Give the position of every Plasmodium parasite.
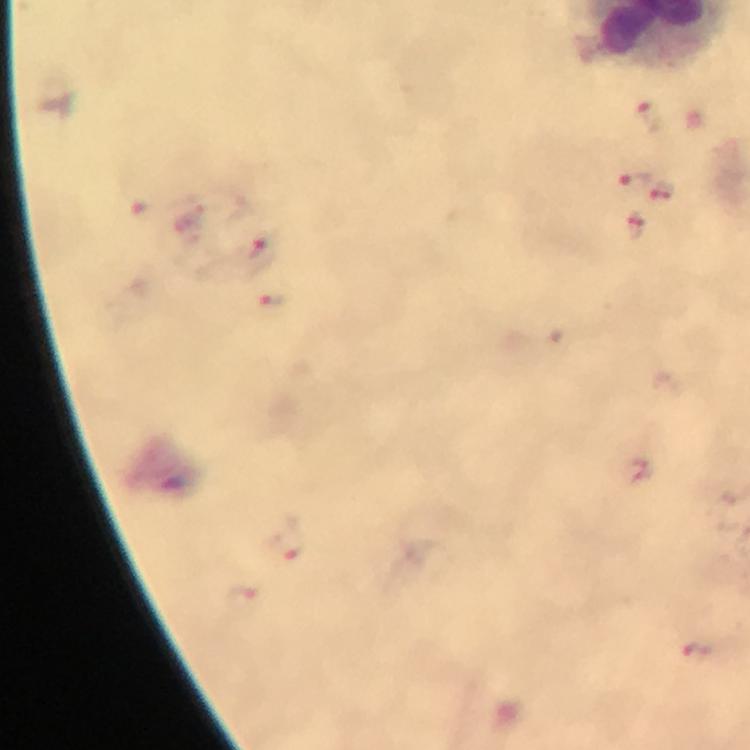

Approximate centers as {x, y} in pixels.
Plasmodium parasites: {649, 115}, {632, 181}, {662, 190}, {635, 225}, {261, 253}, {274, 300}, {284, 540}, {241, 601}, {697, 650}.

100x magnification. Immersion oil was used. Thick smear. Image is 750×750 pixels. Giemsa stain. Photographed through the microscope with a smartphone camera. From a malaria diagnostic workup. Cropped region of a single field of view.